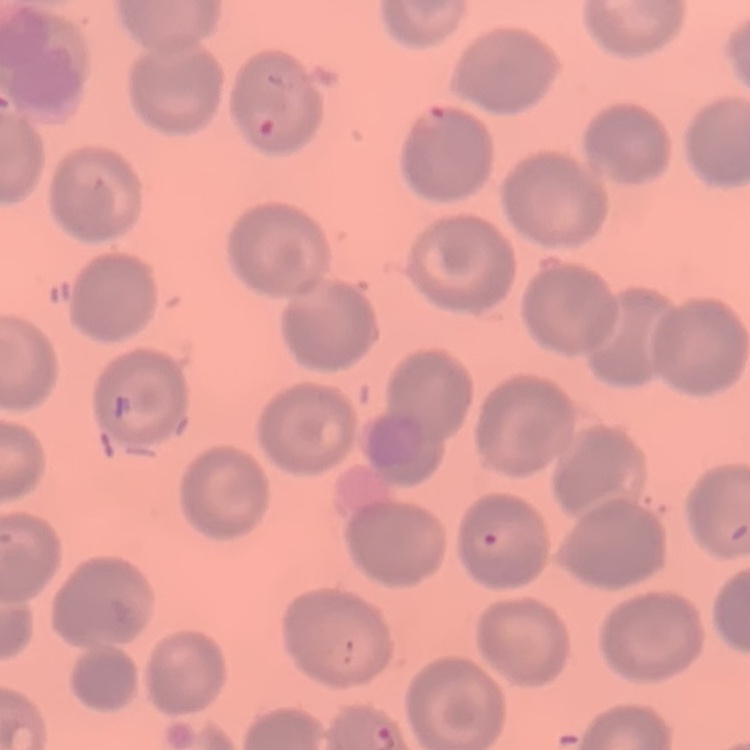
erythrocyte morphology = no rouleaux formation
preparation = thin peripheral smear
image type = square crop of a larger photomicrograph
stain = Field's or Giemsa